State which parasite is depicted.
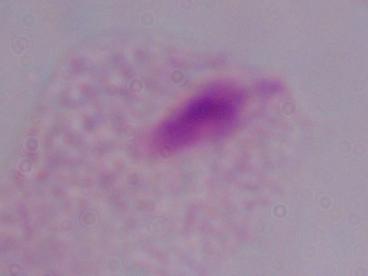
A trichomonad.

Captured at 1000x magnification. Micrograph.